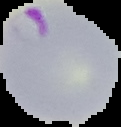

Image is 121×127 pixels. Cell region segmented out of the field of view; the surrounding area is masked to black. Result: malaria parasites identified. From a thin blood smear.